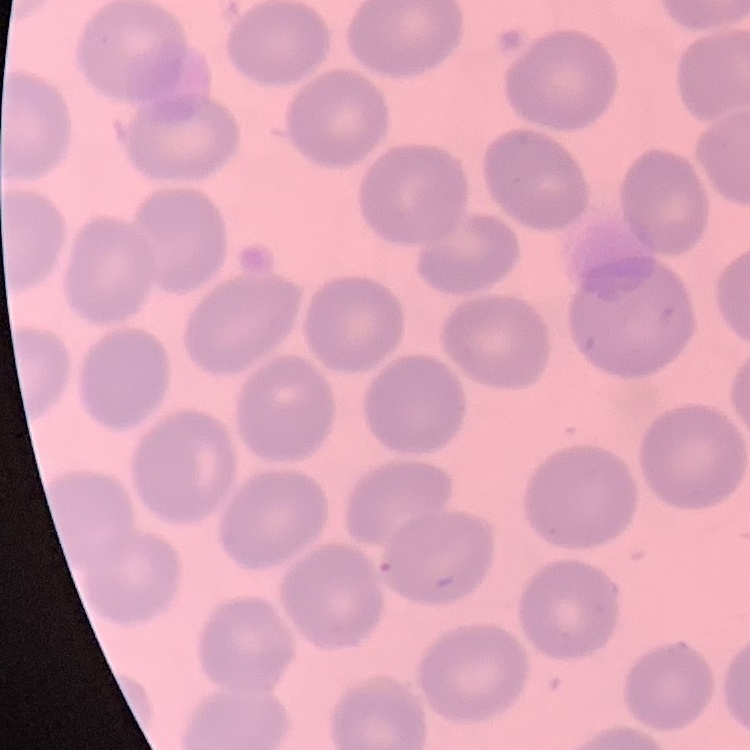
red blood cell morphology = no rouleaux formation
stain = Field's or Giemsa
image type = square crop of a larger photomicrograph
preparation = thin blood smear